Assess this cell for malaria.
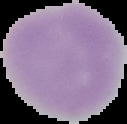
Uninfected.

Segmented cell region on a black background. Image is 127×124 pixels. From a thin blood film.